Assess this cell for malaria.
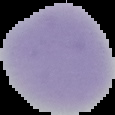

Uninfected.

The area outside the segmented cell region is set to black. Image is 115×115 pixels. From a thin blood smear.